Describe the morphology of the red blood cells.
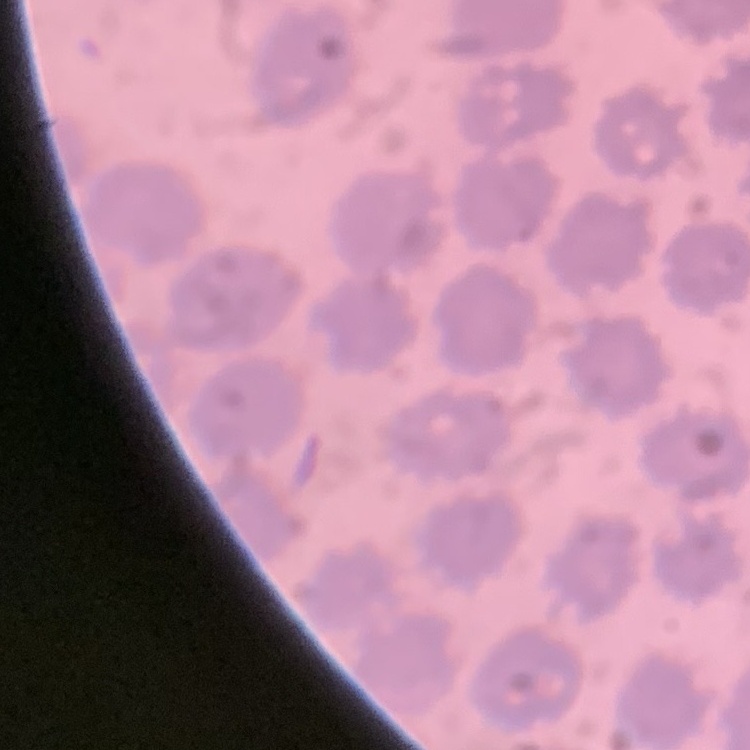

They show no rouleaux formation.

Summary:
  - Stain: Field's or Giemsa
  - Preparation: thin blood smear
  - Image type: one tile cut from a larger photomicrograph